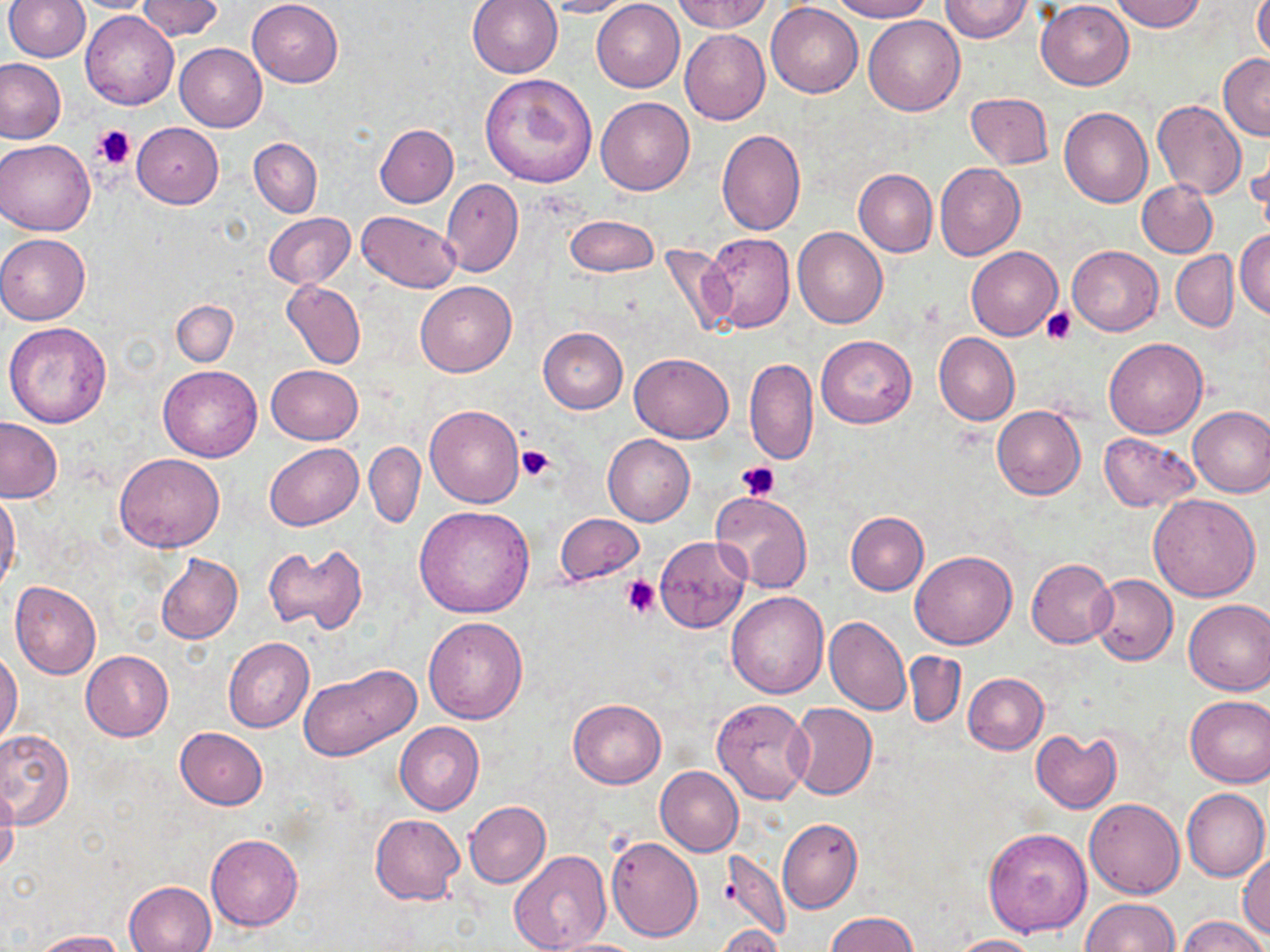 Approximate bounding boxes as (x1, y1, x2, y2) in pixels. Uninfected red blood cell locations: (6, 0, 90, 62), (68, 0, 160, 13), (247, 0, 343, 87), (467, 0, 563, 78), (545, 0, 639, 18), (673, 0, 772, 33), (829, 0, 933, 21), (940, 0, 1034, 42), (1110, 0, 1207, 33), (140, 1, 221, 41), (591, 1, 685, 93), (1035, 1, 1134, 89), (1254, 2, 1270, 64), (767, 3, 862, 98), (81, 11, 180, 110), (864, 16, 965, 117), (680, 28, 770, 125), (174, 44, 266, 131), (1219, 54, 1270, 141), (0, 57, 68, 145), (479, 71, 597, 189), (965, 92, 1054, 169), (596, 97, 694, 195), (1152, 99, 1246, 199), (1059, 105, 1152, 208), (132, 122, 223, 208), (374, 123, 459, 207), (716, 128, 806, 235), (1246, 133, 1269, 227), (250, 138, 322, 217), (0, 139, 95, 235), (935, 163, 1026, 260), (853, 169, 937, 256), (441, 179, 523, 277), (1137, 179, 1217, 257), (356, 210, 460, 292), (264, 213, 354, 287), (565, 216, 658, 276), (792, 228, 888, 328), (1235, 228, 1270, 320), (702, 232, 795, 334), (0, 233, 90, 325), (659, 241, 739, 339), (1067, 245, 1163, 336), (966, 246, 1062, 340), (1171, 250, 1239, 332), (281, 279, 366, 369), (415, 281, 517, 377), (171, 299, 238, 367), (3, 322, 113, 428), (538, 326, 627, 413), (933, 332, 1019, 426), (817, 335, 916, 427), (1104, 337, 1207, 437), (630, 352, 733, 443), (745, 358, 818, 465), (158, 365, 262, 461), (266, 365, 362, 445), (991, 404, 1086, 500), (424, 405, 523, 508), (1187, 405, 1270, 498), (0, 417, 62, 503), (602, 433, 695, 526), (1098, 433, 1199, 510), (364, 441, 426, 530), (264, 443, 362, 531), (114, 454, 223, 553), (0, 491, 21, 596), (708, 491, 811, 594), (1147, 493, 1261, 601), (414, 505, 536, 619), (845, 511, 928, 595), (556, 513, 644, 586), (654, 535, 751, 634), (264, 543, 368, 636), (909, 550, 1017, 648), (154, 552, 243, 645), (1027, 558, 1116, 648), (1089, 573, 1178, 665), (10, 581, 101, 681), (725, 591, 830, 698), (1183, 598, 1270, 696), (824, 615, 911, 715), (422, 616, 529, 724), (224, 637, 314, 732), (0, 649, 23, 745), (81, 650, 173, 739), (905, 651, 966, 727), (297, 663, 420, 761), (963, 672, 1049, 754), (1185, 695, 1270, 787), (568, 697, 666, 788), (711, 698, 812, 804), (787, 703, 878, 799), (395, 722, 485, 815), (175, 727, 268, 809), (0, 730, 74, 829), (1031, 731, 1121, 813), (655, 766, 744, 856), (0, 788, 20, 874), (1182, 788, 1268, 882), (1085, 797, 1185, 899), (464, 801, 551, 888), (369, 814, 465, 905), (778, 818, 863, 914), (983, 827, 1094, 937), (206, 835, 302, 931), (607, 836, 702, 941), (718, 847, 790, 940), (509, 851, 613, 952), (1237, 854, 1270, 940), (124, 880, 217, 951), (1079, 898, 1181, 952), (824, 912, 919, 952), (1179, 916, 1266, 952), (715, 925, 785, 952), (32, 929, 124, 951), (947, 934, 1039, 952), (540, 938, 652, 952). Platelet locations: (93, 124, 137, 168), (1042, 308, 1075, 345), (516, 444, 555, 482), (736, 460, 780, 501), (622, 575, 660, 618). Slide-level diagnosis: negative for blood parasites. May-Grünwald-Giemsa stain. Optical microscopy. Single field of view. Thin blood film. Image is 1270×952 pixels. 1000x magnification.